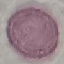

Malaria status: uninfected. Photographed with a smartphone camera at the microscope eyepiece. Giemsa stain. Automatically extracted cell patch, resized to 64 × 64 pixels. Thin blood film.